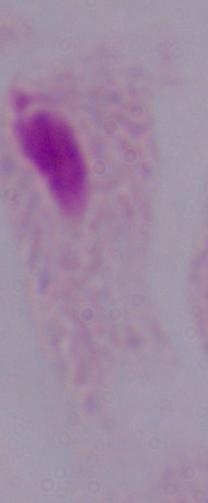
Summary:
  - Identification: trichomonad
  - Magnification: 1000x
  - Modality: photomicrograph